Locate every malaria parasite.
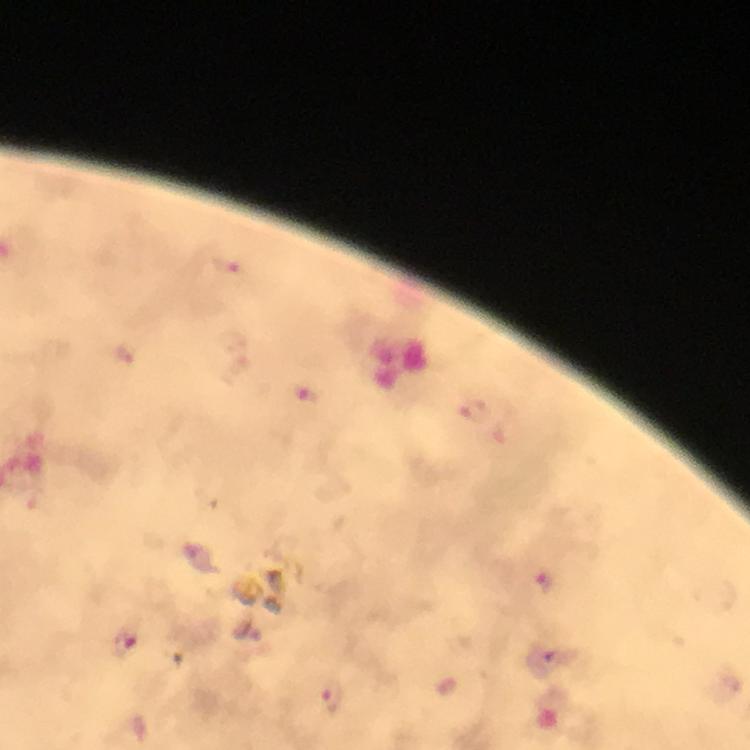

Approximate object centers, in pixels from the top-left corner.
Malaria parasites: (x=226, y=265), (x=125, y=355), (x=309, y=395), (x=475, y=413), (x=545, y=582), (x=123, y=643), (x=332, y=700).

{
  "magnification": "100x",
  "image_size": "750×750 pixels",
  "context": "from a diagnostic examination for malaria",
  "preparation": "thick blood film",
  "capture": "smartphone mounted on the microscope",
  "immersion_oil": "used",
  "cropped_from": "a single field of view",
  "stain": "Giemsa"
}